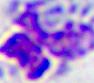
Summary:
  - Modality: micrograph
  - Magnification: 400x
  - Identification: leukocyte